Name the cell type shown.
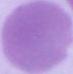

An erythrocyte.

Photomicrograph. 1000x magnification.